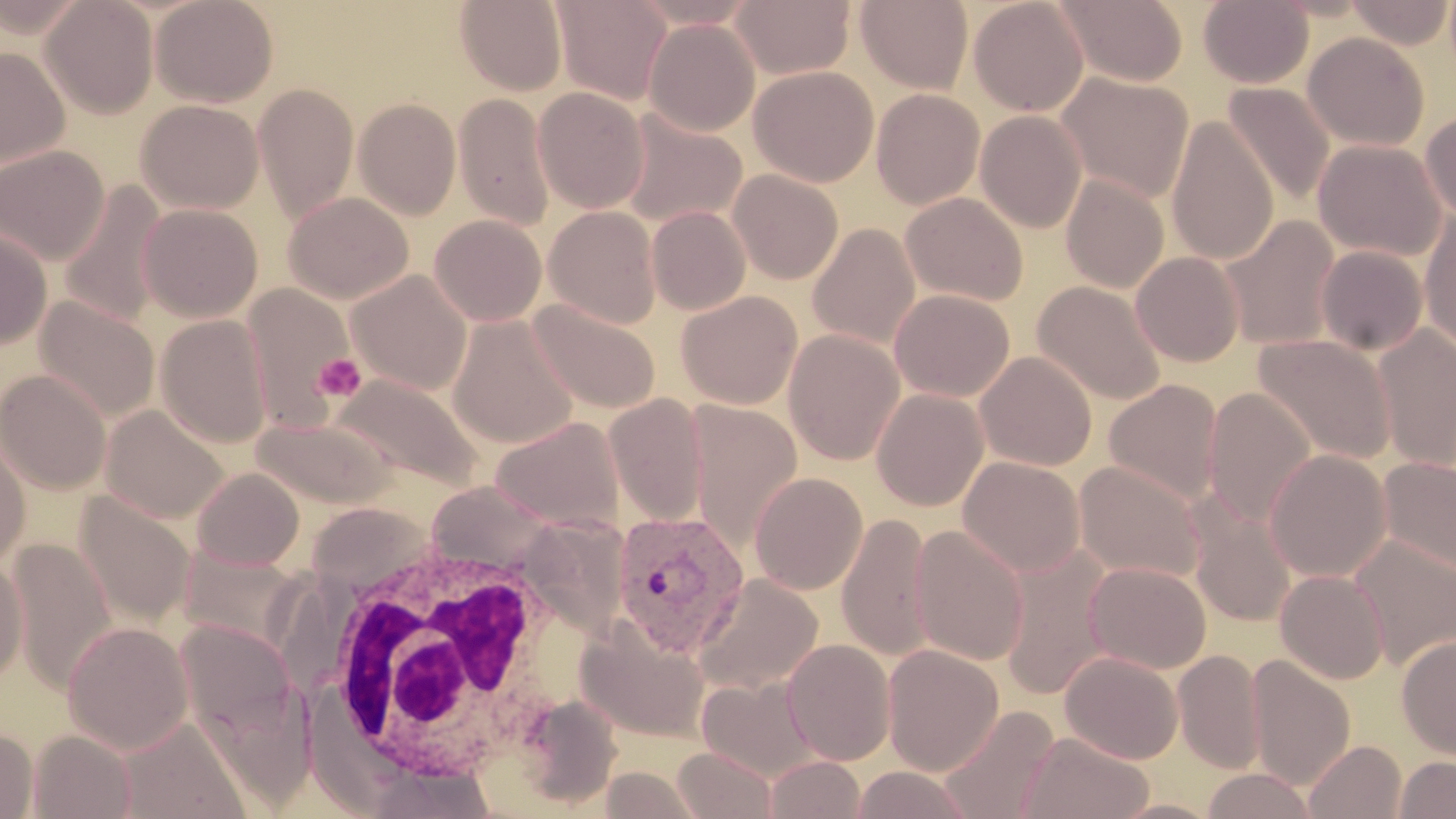 Approximate bounding boxes as named x1/y1/x2/y2 corners in pixels. Plasmodium vivax-infected red blood cell locations: (x1=611, y1=509, x2=751, y2=658). Platelet locations: (x1=313, y1=352, x2=366, y2=403). White blood cell locations: (x1=311, y1=525, x2=582, y2=787). Uninfected red blood cell locations: (x1=40, y1=0, x2=159, y2=119), (x1=151, y1=0, x2=279, y2=108), (x1=552, y1=0, x2=672, y2=105), (x1=731, y1=0, x2=855, y2=80), (x1=855, y1=0, x2=974, y2=93), (x1=968, y1=0, x2=1089, y2=116), (x1=1054, y1=0, x2=1189, y2=86), (x1=1198, y1=0, x2=1314, y2=89), (x1=1346, y1=0, x2=1454, y2=49), (x1=455, y1=1, x2=567, y2=95), (x1=644, y1=18, x2=760, y2=136), (x1=1303, y1=32, x2=1430, y2=151), (x1=0, y1=46, x2=69, y2=169), (x1=748, y1=65, x2=879, y2=187), (x1=1055, y1=73, x2=1194, y2=204), (x1=253, y1=83, x2=359, y2=223), (x1=1222, y1=83, x2=1335, y2=208), (x1=533, y1=86, x2=650, y2=214), (x1=871, y1=88, x2=985, y2=209), (x1=453, y1=92, x2=556, y2=231), (x1=353, y1=98, x2=461, y2=219), (x1=136, y1=99, x2=264, y2=214), (x1=618, y1=109, x2=748, y2=229), (x1=975, y1=110, x2=1087, y2=233), (x1=1420, y1=111, x2=1456, y2=222), (x1=1166, y1=114, x2=1279, y2=266), (x1=1312, y1=139, x2=1447, y2=262), (x1=0, y1=145, x2=110, y2=264), (x1=728, y1=168, x2=843, y2=284), (x1=1060, y1=174, x2=1169, y2=293), (x1=58, y1=181, x2=168, y2=329), (x1=284, y1=191, x2=414, y2=304), (x1=900, y1=191, x2=1028, y2=306), (x1=137, y1=204, x2=262, y2=322), (x1=544, y1=205, x2=663, y2=329), (x1=647, y1=206, x2=751, y2=315), (x1=1419, y1=209, x2=1456, y2=351), (x1=429, y1=215, x2=547, y2=326), (x1=1219, y1=216, x2=1341, y2=352), (x1=807, y1=222, x2=921, y2=350), (x1=0, y1=225, x2=52, y2=349), (x1=1316, y1=245, x2=1428, y2=356), (x1=1131, y1=252, x2=1245, y2=367), (x1=347, y1=269, x2=472, y2=395), (x1=1032, y1=280, x2=1167, y2=406), (x1=243, y1=283, x2=356, y2=429), (x1=889, y1=289, x2=1015, y2=402), (x1=676, y1=290, x2=802, y2=409), (x1=34, y1=296, x2=160, y2=422), (x1=528, y1=299, x2=662, y2=415), (x1=155, y1=314, x2=273, y2=448), (x1=447, y1=315, x2=579, y2=448), (x1=1373, y1=324, x2=1456, y2=472), (x1=783, y1=329, x2=905, y2=466), (x1=1252, y1=333, x2=1396, y2=467), (x1=975, y1=351, x2=1097, y2=471), (x1=0, y1=369, x2=112, y2=495), (x1=332, y1=373, x2=483, y2=492), (x1=1103, y1=378, x2=1224, y2=506), (x1=871, y1=388, x2=989, y2=511), (x1=1203, y1=388, x2=1318, y2=528), (x1=603, y1=393, x2=709, y2=528), (x1=684, y1=401, x2=803, y2=551), (x1=100, y1=404, x2=230, y2=523), (x1=252, y1=415, x2=398, y2=509), (x1=490, y1=416, x2=626, y2=531), (x1=0, y1=428, x2=31, y2=568), (x1=1263, y1=449, x2=1392, y2=582), (x1=958, y1=456, x2=1085, y2=577), (x1=1377, y1=456, x2=1456, y2=576), (x1=1073, y1=460, x2=1206, y2=584), (x1=192, y1=467, x2=305, y2=570), (x1=749, y1=472, x2=868, y2=595), (x1=75, y1=491, x2=196, y2=630), (x1=1187, y1=499, x2=1296, y2=627), (x1=836, y1=513, x2=935, y2=662), (x1=909, y1=524, x2=1030, y2=666), (x1=1348, y1=533, x2=1456, y2=668), (x1=7, y1=540, x2=118, y2=692), (x1=178, y1=544, x2=307, y2=652), (x1=997, y1=545, x2=1115, y2=702), (x1=0, y1=554, x2=28, y2=686), (x1=1084, y1=561, x2=1211, y2=674), (x1=1275, y1=569, x2=1389, y2=684), (x1=694, y1=573, x2=824, y2=692), (x1=575, y1=616, x2=711, y2=742), (x1=173, y1=619, x2=300, y2=745), (x1=62, y1=621, x2=194, y2=755), (x1=1396, y1=634, x2=1456, y2=760), (x1=782, y1=639, x2=896, y2=766), (x1=882, y1=644, x2=1004, y2=775), (x1=1173, y1=649, x2=1266, y2=773), (x1=1060, y1=650, x2=1184, y2=764), (x1=1246, y1=654, x2=1356, y2=790), (x1=696, y1=673, x2=822, y2=782), (x1=516, y1=692, x2=624, y2=808), (x1=935, y1=704, x2=1060, y2=819), (x1=116, y1=716, x2=251, y2=819), (x1=0, y1=727, x2=38, y2=818), (x1=28, y1=729, x2=136, y2=818), (x1=1019, y1=731, x2=1154, y2=818), (x1=1302, y1=739, x2=1406, y2=819), (x1=673, y1=746, x2=777, y2=818), (x1=763, y1=755, x2=867, y2=819), (x1=1394, y1=756, x2=1456, y2=818), (x1=357, y1=760, x2=500, y2=817), (x1=850, y1=766, x2=974, y2=818), (x1=1199, y1=768, x2=1320, y2=818). Slide-level diagnosis: Plasmodium vivax. Light microscopy. Captured at 1000x magnification. Thin blood film. May-Grünwald-Giemsa-stained preparation. Single field of view. Image is 1456×819 pixels.